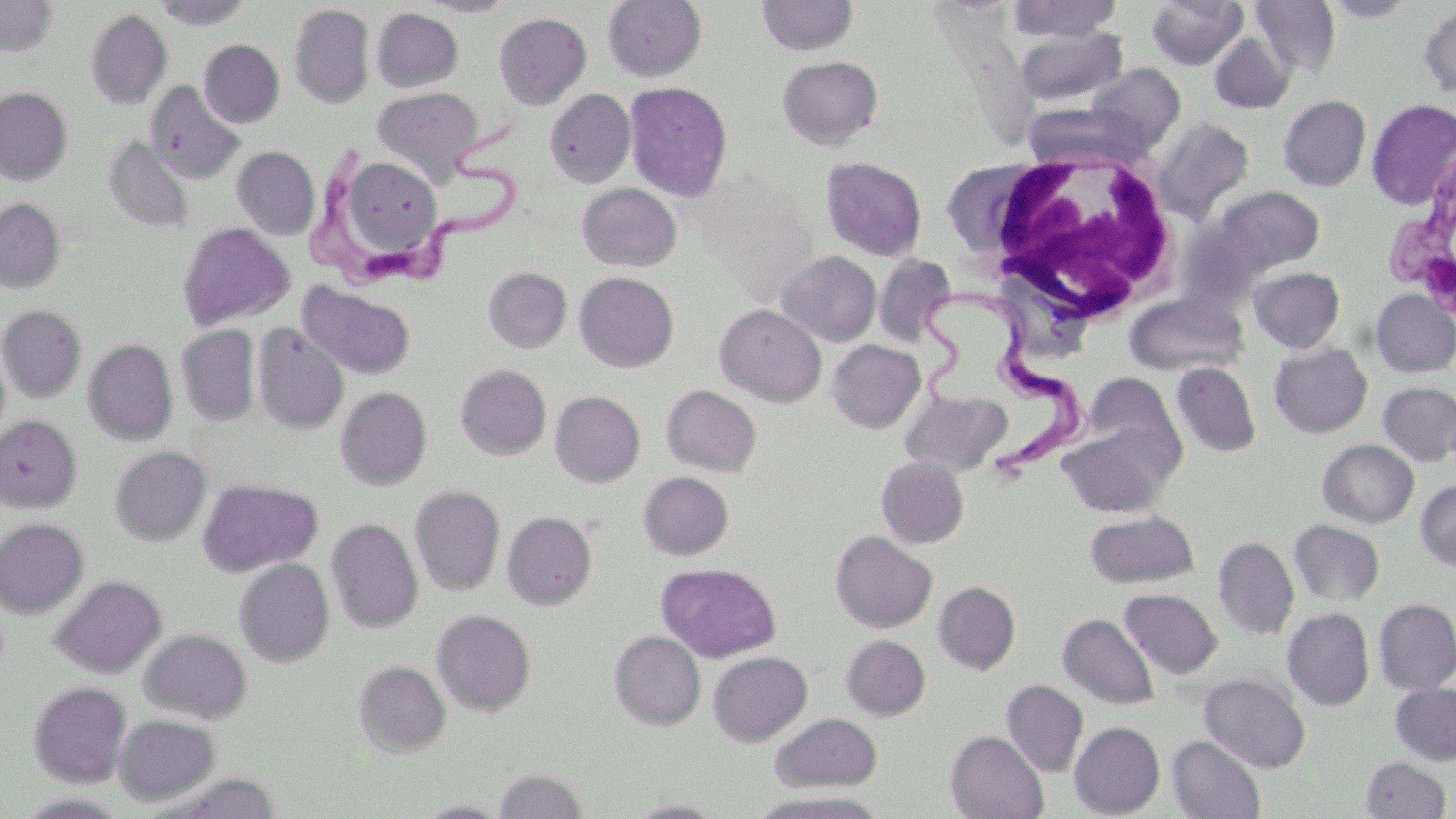

slide-level diagnosis = Trypanosoma brucei
image size = 1456×819 pixels
field of view = single
uninfected red blood cell locations = approximate bounding boxes as named x1/y1/x2/y2 corners in pixels: (x1=0, y1=0, x2=60, y2=56), (x1=151, y1=0, x2=255, y2=29), (x1=414, y1=0, x2=516, y2=17), (x1=603, y1=0, x2=707, y2=82), (x1=756, y1=0, x2=859, y2=56), (x1=1005, y1=0, x2=1124, y2=42), (x1=1146, y1=0, x2=1248, y2=71), (x1=1250, y1=0, x2=1341, y2=79), (x1=1320, y1=0, x2=1420, y2=21), (x1=1418, y1=1, x2=1456, y2=99), (x1=289, y1=4, x2=375, y2=109), (x1=371, y1=7, x2=464, y2=92), (x1=85, y1=9, x2=173, y2=109), (x1=493, y1=13, x2=591, y2=109), (x1=1015, y1=27, x2=1129, y2=108), (x1=1209, y1=33, x2=1296, y2=113), (x1=199, y1=39, x2=285, y2=128), (x1=776, y1=56, x2=883, y2=150), (x1=1086, y1=62, x2=1186, y2=152), (x1=145, y1=80, x2=245, y2=185), (x1=624, y1=81, x2=733, y2=202), (x1=371, y1=86, x2=484, y2=186), (x1=0, y1=88, x2=73, y2=185), (x1=545, y1=89, x2=635, y2=187), (x1=1278, y1=95, x2=1371, y2=191), (x1=1366, y1=98, x2=1456, y2=211), (x1=1153, y1=117, x2=1255, y2=223), (x1=102, y1=135, x2=195, y2=234), (x1=232, y1=146, x2=319, y2=240), (x1=340, y1=152, x2=448, y2=260), (x1=821, y1=156, x2=927, y2=261), (x1=577, y1=183, x2=682, y2=272), (x1=1215, y1=186, x2=1325, y2=275), (x1=0, y1=198, x2=65, y2=293), (x1=176, y1=221, x2=296, y2=331), (x1=776, y1=251, x2=881, y2=346), (x1=874, y1=254, x2=956, y2=346), (x1=1249, y1=266, x2=1345, y2=353), (x1=483, y1=267, x2=571, y2=352), (x1=574, y1=272, x2=679, y2=372), (x1=297, y1=282, x2=416, y2=380), (x1=1371, y1=290, x2=1456, y2=378), (x1=1125, y1=292, x2=1247, y2=378), (x1=715, y1=304, x2=827, y2=407), (x1=0, y1=305, x2=86, y2=403), (x1=252, y1=324, x2=348, y2=435), (x1=176, y1=325, x2=260, y2=427), (x1=84, y1=339, x2=178, y2=446), (x1=828, y1=339, x2=925, y2=433), (x1=1269, y1=342, x2=1372, y2=439), (x1=1171, y1=362, x2=1261, y2=457), (x1=455, y1=364, x2=551, y2=460), (x1=1081, y1=372, x2=1186, y2=468), (x1=1377, y1=381, x2=1456, y2=467), (x1=661, y1=384, x2=762, y2=476), (x1=336, y1=386, x2=431, y2=490), (x1=901, y1=388, x2=1012, y2=478), (x1=550, y1=390, x2=645, y2=488), (x1=0, y1=415, x2=82, y2=512), (x1=1057, y1=420, x2=1179, y2=519), (x1=1317, y1=439, x2=1418, y2=528), (x1=110, y1=445, x2=211, y2=546), (x1=877, y1=456, x2=969, y2=549), (x1=638, y1=471, x2=734, y2=560), (x1=198, y1=477, x2=323, y2=577), (x1=1415, y1=479, x2=1456, y2=571), (x1=410, y1=486, x2=505, y2=596), (x1=502, y1=511, x2=597, y2=610), (x1=1085, y1=511, x2=1200, y2=589), (x1=0, y1=518, x2=89, y2=618), (x1=326, y1=518, x2=422, y2=633), (x1=1289, y1=520, x2=1385, y2=606), (x1=830, y1=530, x2=937, y2=633), (x1=1213, y1=536, x2=1299, y2=641), (x1=234, y1=559, x2=334, y2=666), (x1=657, y1=562, x2=780, y2=661), (x1=50, y1=575, x2=166, y2=678), (x1=934, y1=581, x2=1020, y2=674), (x1=1120, y1=588, x2=1222, y2=679), (x1=1373, y1=598, x2=1456, y2=694), (x1=1283, y1=608, x2=1375, y2=710), (x1=431, y1=609, x2=536, y2=717), (x1=1058, y1=613, x2=1159, y2=709), (x1=139, y1=628, x2=252, y2=723), (x1=609, y1=631, x2=706, y2=730), (x1=841, y1=635, x2=930, y2=720), (x1=708, y1=651, x2=812, y2=745), (x1=353, y1=660, x2=451, y2=757), (x1=1198, y1=673, x2=1311, y2=773), (x1=1002, y1=679, x2=1088, y2=777), (x1=28, y1=681, x2=131, y2=786), (x1=1390, y1=683, x2=1456, y2=765), (x1=114, y1=713, x2=220, y2=805), (x1=770, y1=713, x2=883, y2=792), (x1=1069, y1=721, x2=1165, y2=818), (x1=946, y1=731, x2=1049, y2=819), (x1=1167, y1=735, x2=1266, y2=818), (x1=1360, y1=757, x2=1452, y2=819), (x1=493, y1=768, x2=590, y2=818), (x1=745, y1=791, x2=891, y2=818), (x1=626, y1=798, x2=729, y2=818), (x1=414, y1=800, x2=512, y2=818)
modality = optical microscopy
magnification = 1000x
preparation = thin blood smear
stain = May-Grünwald-Giemsa
Trypanosoma brucei locations = approximate bounding boxes as named x1/y1/x2/y2 corners in pixels: (x1=307, y1=121, x2=523, y2=296), (x1=1381, y1=147, x2=1456, y2=317), (x1=906, y1=286, x2=1086, y2=477)
white blood cell locations = approximate bounding boxes as named x1/y1/x2/y2 corners in pixels: (x1=977, y1=152, x2=1183, y2=324)